State the blood parasite species.
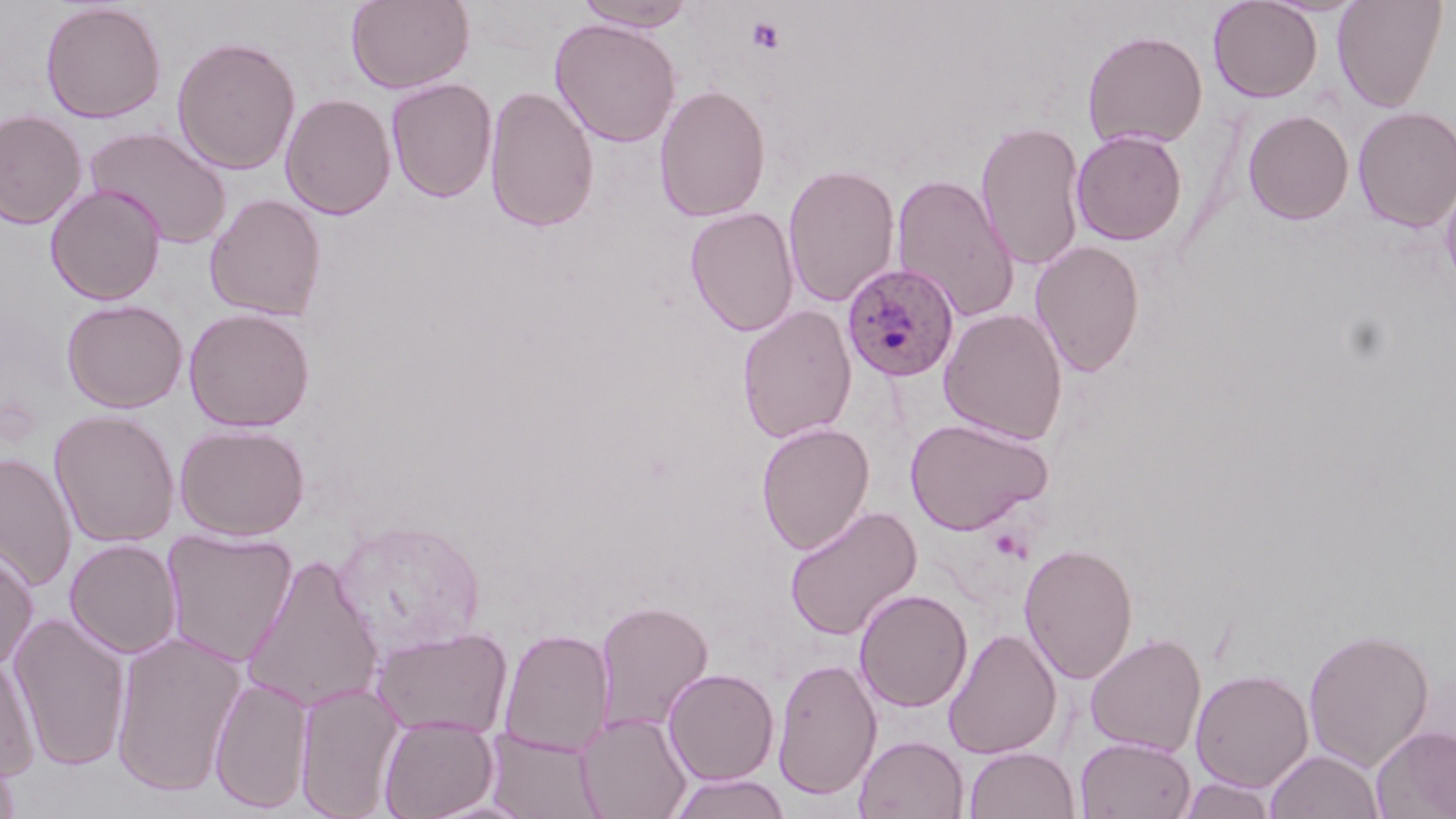

Plasmodium ovale.

Summary:
  - Coordinate format: approximate bounding boxes as [x1, y1, x2, y2] in pixels
  - Plasmodium ovale-infected red blood cell locations: [841, 261, 960, 383]
  - Uninfected red blood cell locations: [345, 0, 474, 93], [574, 0, 698, 32], [1208, 0, 1322, 102], [1332, 0, 1448, 111], [40, 2, 166, 124], [549, 17, 682, 148], [1082, 29, 1208, 149], [171, 35, 302, 176], [385, 77, 498, 203], [654, 83, 772, 222], [483, 84, 600, 233], [279, 92, 396, 220], [1352, 105, 1456, 232], [0, 109, 88, 229], [1242, 109, 1355, 225], [975, 119, 1087, 272], [85, 125, 232, 249], [1071, 129, 1188, 246], [783, 163, 901, 308], [891, 172, 1019, 324], [1440, 174, 1456, 293], [46, 184, 166, 305], [204, 193, 327, 321], [684, 206, 800, 336], [1030, 239, 1146, 376], [61, 298, 188, 413], [737, 305, 857, 444], [183, 307, 316, 432], [938, 308, 1069, 445], [48, 409, 181, 548], [904, 417, 1053, 535], [756, 421, 875, 555], [174, 423, 310, 541], [0, 452, 78, 591], [784, 505, 922, 640], [331, 518, 486, 658], [161, 527, 298, 667], [65, 539, 182, 660], [1019, 541, 1139, 684], [0, 547, 39, 671], [240, 553, 385, 713], [853, 589, 973, 712], [594, 599, 713, 736], [7, 612, 132, 771], [370, 625, 513, 740], [1303, 626, 1435, 772], [499, 627, 614, 756], [943, 627, 1062, 759], [110, 630, 247, 797], [1085, 632, 1206, 757], [0, 653, 40, 781], [772, 657, 882, 800], [663, 668, 779, 785], [1190, 669, 1314, 792], [209, 674, 314, 813], [295, 681, 406, 818], [576, 711, 691, 819], [378, 713, 499, 819], [1372, 724, 1456, 819], [485, 728, 605, 819], [854, 734, 969, 819], [1076, 735, 1195, 818], [964, 746, 1080, 819], [0, 748, 22, 819], [1265, 749, 1384, 819], [668, 772, 791, 819], [1177, 775, 1277, 819]
  - Platelet locations: [745, 15, 786, 54]
  - Stain: May-Grünwald-Giemsa
  - Modality: light microscopy
  - Preparation: thin blood film
  - Field of view: single
  - Magnification: 1000x
  - Image size: 1456×819 pixels